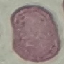

malaria status = uninfected
preparation = thin smear
capture = smartphone through the microscope eyepiece
stain = Giemsa
image type = automatically extracted cell patch, resized to 64 × 64 pixels